Comment on the morphology of the red blood cells.
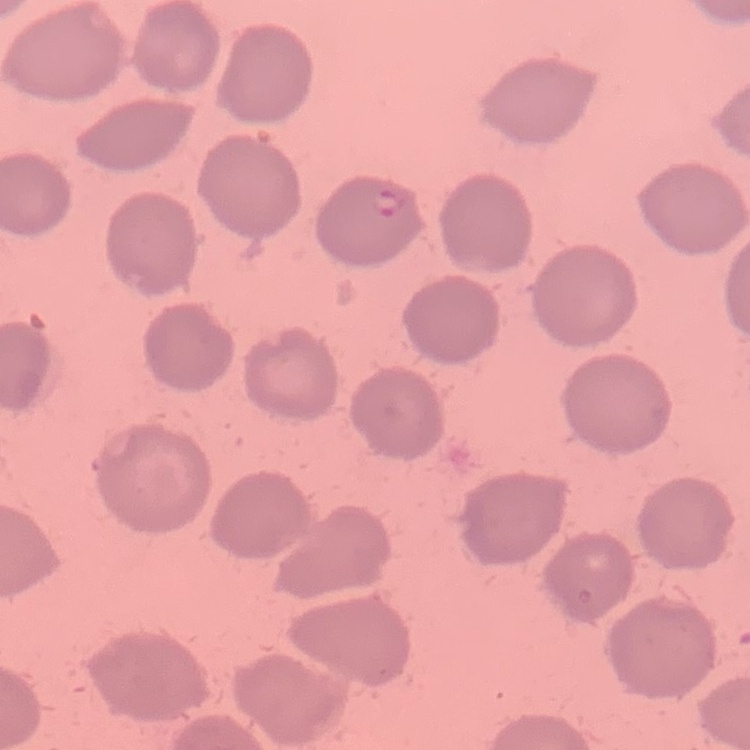

They show no rouleaux formation.

Square crop of a larger photomicrograph. Field's or Giemsa stain. Thin blood smear.